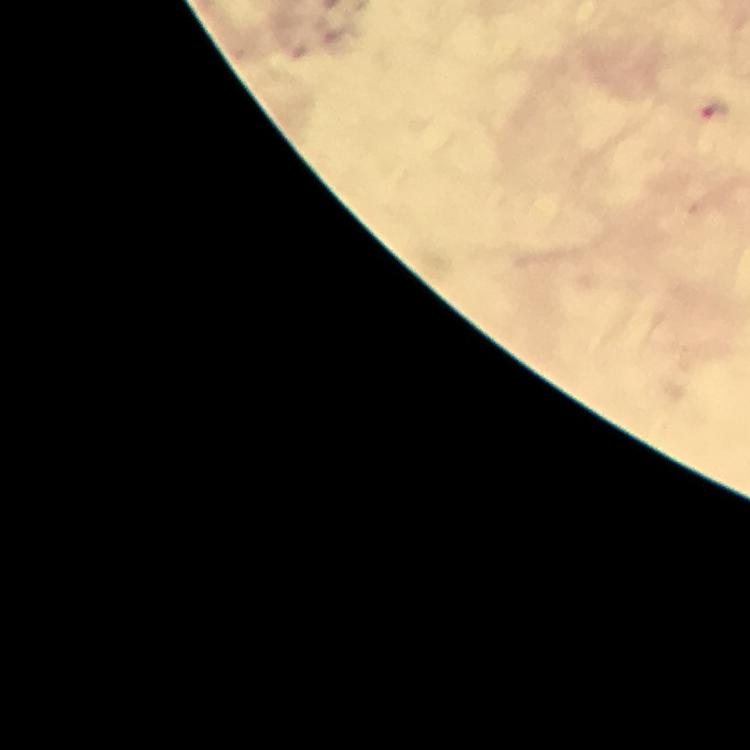

preparation: thick blood film
magnification: 100x
capture: smartphone mounted on the microscope
stain: Giemsa
immersion_oil: applied
malaria_parasite_locations: 'approximate centers as [x, y] in pixels: [715, 112]'
cropped_from: a single field of view
context: from a diagnostic examination for malaria
image_size: 750×750 pixels